Assess this cell for malaria.
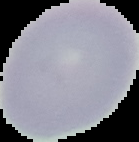

It is uninfected.

Summary:
  - Image type: cell region segmented out of the field of view; surrounding area masked to black
  - Image size: 139×142 pixels
  - Preparation: thin blood film